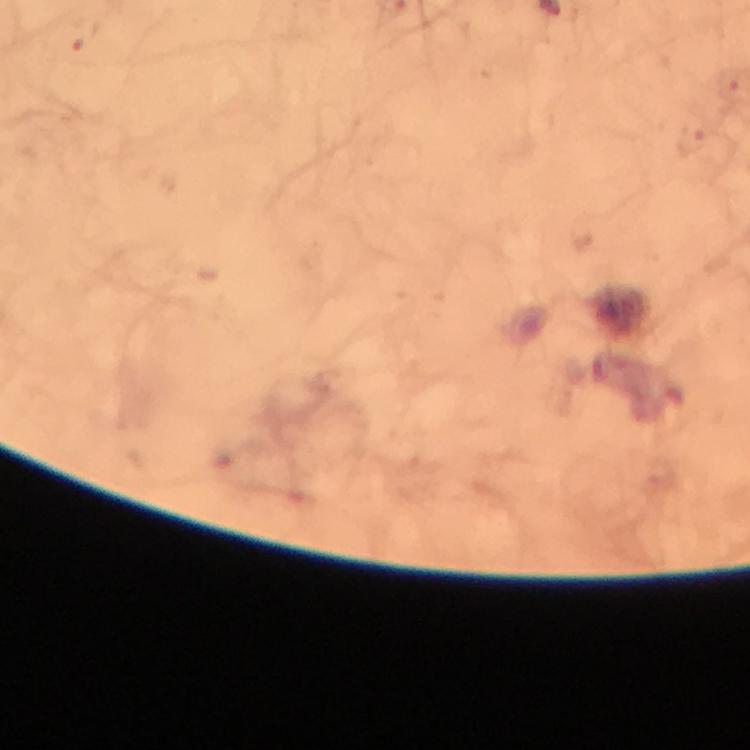 Approximate centers as (x, y) in pixels. Malaria parasite locations: (84, 33), (690, 140). Smartphone photograph taken through a microscope. Immersion oil applied. Giemsa stain. Thick smear. Cropped region of a single field of view. At 100x magnification. From a malaria diagnostic workup. Image is 750×750 pixels.